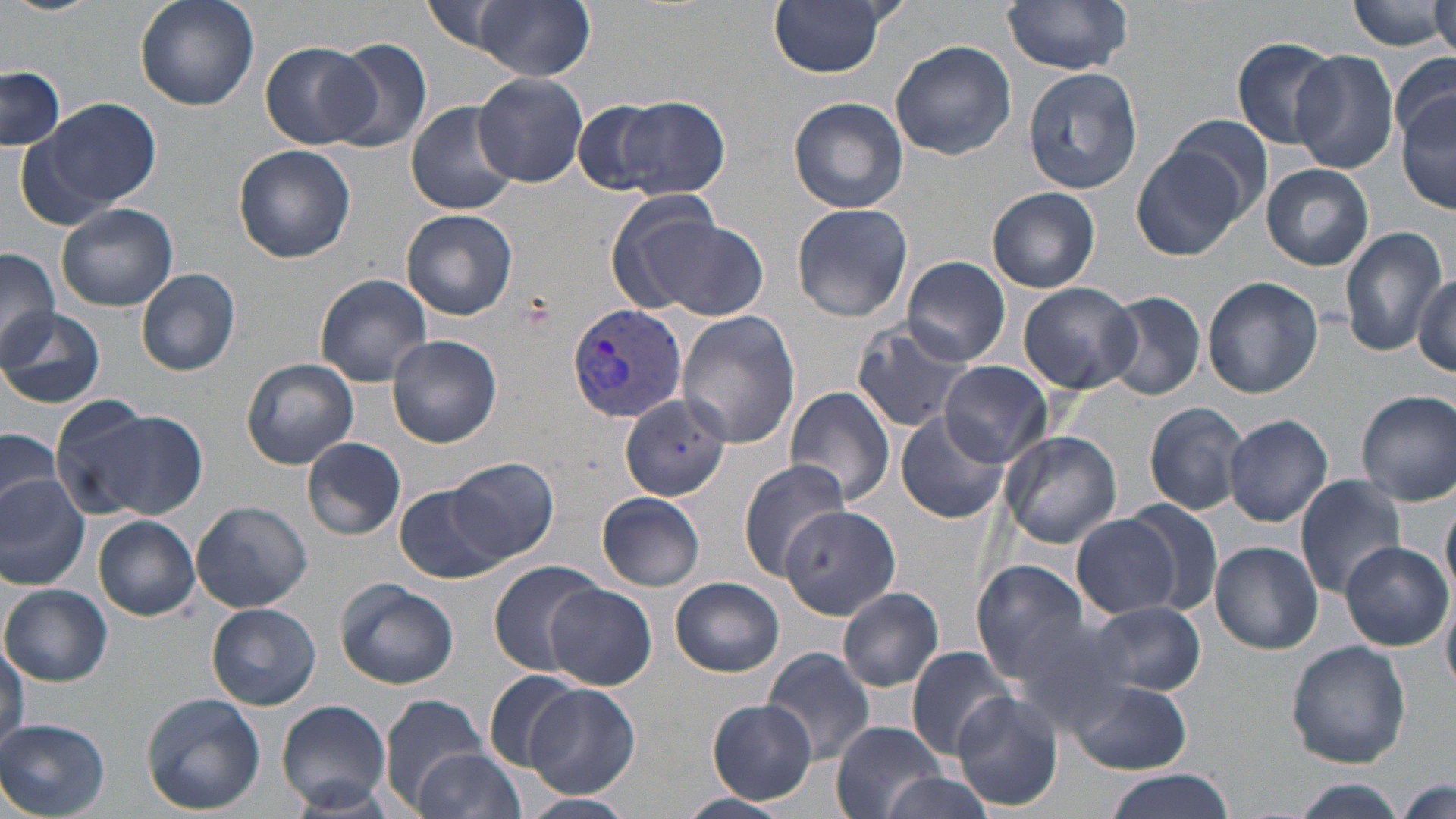
Summary:
  - Coordinate format: approximate bounding boxes as [x1, y1, x2, y2] in pixels
  - Plasmodium vivax-infected red blood cell locations: [565, 302, 691, 421]
  - Uninfected red blood cell locations: [132, 0, 259, 111], [423, 0, 522, 55], [769, 0, 892, 77], [1003, 0, 1135, 74], [1348, 0, 1448, 52], [1429, 0, 1456, 58], [472, 1, 595, 80], [1233, 36, 1342, 149], [325, 38, 433, 154], [261, 40, 374, 149], [890, 40, 1017, 161], [1290, 48, 1399, 174], [1389, 53, 1455, 144], [0, 66, 67, 151], [1023, 66, 1143, 194], [474, 71, 588, 187], [1398, 94, 1456, 213], [612, 96, 729, 200], [787, 96, 909, 214], [34, 97, 162, 214], [406, 99, 518, 215], [573, 100, 668, 194], [1167, 115, 1273, 216], [233, 145, 356, 263], [1132, 145, 1247, 261], [1262, 163, 1374, 270], [987, 187, 1100, 293], [57, 202, 178, 311], [791, 203, 913, 322], [402, 209, 518, 321], [632, 215, 770, 321], [1338, 224, 1448, 359], [0, 247, 59, 366], [902, 256, 1009, 365], [136, 268, 241, 376], [1413, 271, 1455, 373], [313, 272, 435, 386], [1203, 276, 1323, 398], [1018, 282, 1140, 394], [1101, 291, 1206, 401], [1, 309, 105, 408], [676, 311, 800, 448], [849, 322, 970, 433], [387, 335, 501, 449], [240, 357, 359, 469], [938, 361, 1053, 467], [784, 386, 896, 506], [1356, 389, 1456, 505], [621, 394, 730, 502], [55, 402, 202, 521], [1145, 402, 1248, 514], [896, 410, 1011, 525], [1214, 410, 1448, 517], [1224, 413, 1333, 527], [0, 428, 64, 510], [1000, 429, 1124, 549], [301, 437, 406, 542], [448, 457, 560, 564], [737, 459, 850, 579], [0, 473, 93, 590], [1294, 475, 1408, 599], [394, 484, 504, 584], [1442, 488, 1456, 601], [598, 492, 706, 591], [575, 497, 696, 659], [190, 498, 313, 614], [1121, 498, 1225, 616], [785, 504, 911, 629], [1071, 514, 1182, 618], [93, 515, 200, 620], [1211, 541, 1323, 653], [1340, 541, 1450, 650], [969, 557, 1093, 681], [489, 561, 605, 676], [671, 577, 785, 677], [334, 579, 460, 689], [544, 583, 655, 690], [2, 584, 114, 686], [838, 586, 944, 691], [1442, 590, 1456, 700], [1087, 600, 1206, 695], [206, 602, 321, 711], [999, 610, 1143, 729], [0, 640, 28, 753], [1285, 642, 1410, 769], [905, 646, 1019, 758], [761, 648, 876, 764], [482, 670, 583, 772], [1064, 677, 1192, 774], [525, 682, 640, 796], [951, 691, 1064, 811], [142, 693, 265, 814], [378, 693, 489, 809], [278, 700, 390, 815], [708, 700, 817, 803], [0, 719, 111, 817], [830, 722, 950, 817], [414, 742, 525, 819], [1103, 771, 1235, 819], [879, 772, 997, 819], [1282, 778, 1411, 818], [1393, 779, 1454, 818], [521, 793, 636, 817], [677, 793, 792, 819]
  - Slide-level diagnosis: Plasmodium vivax
  - Field of view: single
  - Modality: light microscopy
  - Preparation: thin blood film
  - Stain: May-Grünwald-Giemsa
  - Image size: 1456×819 pixels
  - Magnification: 1000x